State which cell type is depicted.
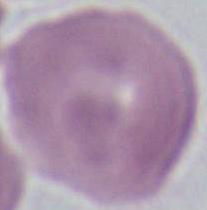

An erythrocyte.

Summary:
  - Magnification: 1000x
  - Modality: micrograph